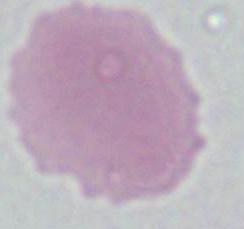
Summary:
  - Magnification: 1000x
  - Modality: micrograph
  - Identification: erythrocyte